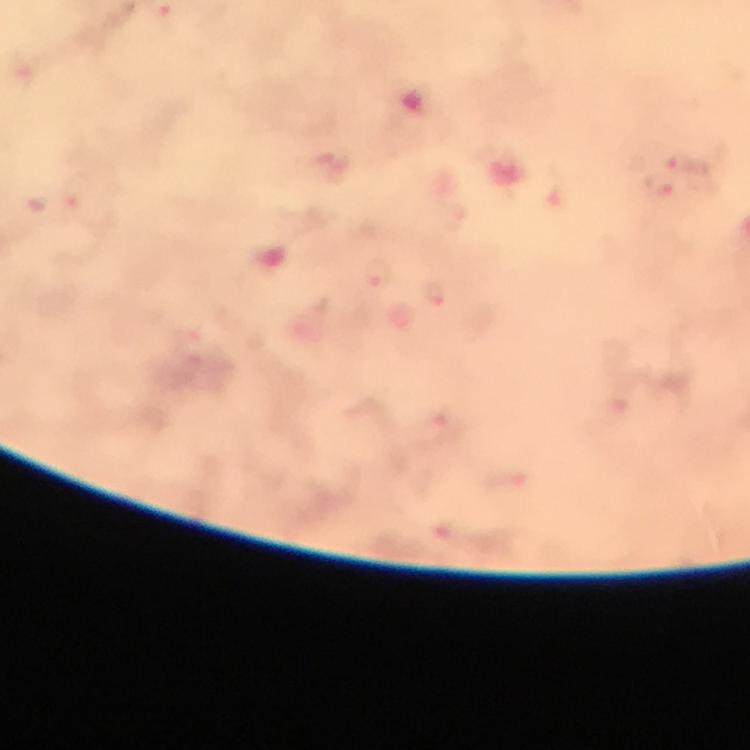 Approximate centers as {x, y} in pixels. Malaria parasite locations: {682, 166}, {376, 273}, {435, 292}. Immersion oil applied. At 100x magnification. Giemsa stain. Image is 750×750 pixels. A crop from one field of view. From a diagnostic examination for malaria. Photographed with a smartphone mounted on the microscope. Thick blood film.